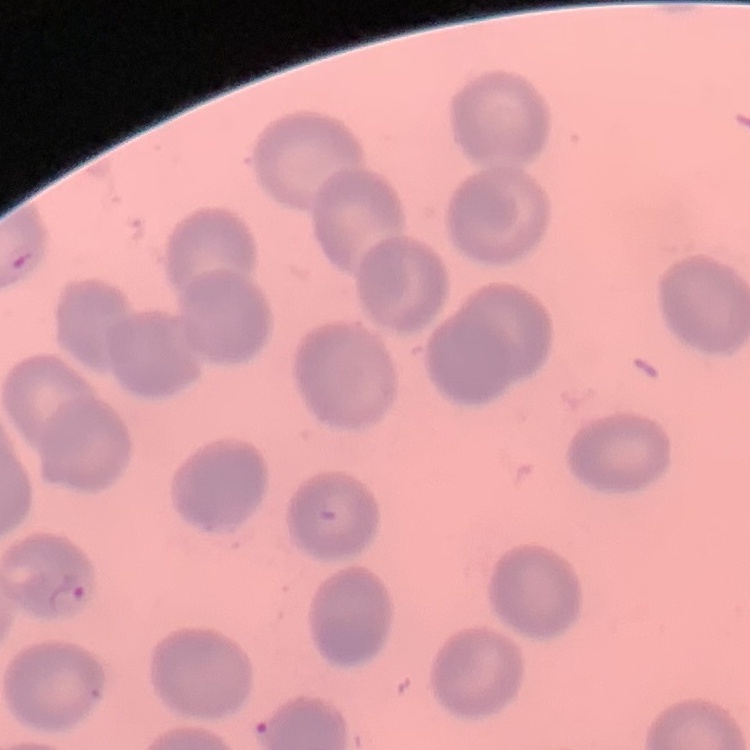

The erythrocytes exhibit no rouleaux formation. Square crop of a larger photomicrograph. Thin blood film. Field's or Giemsa stain.